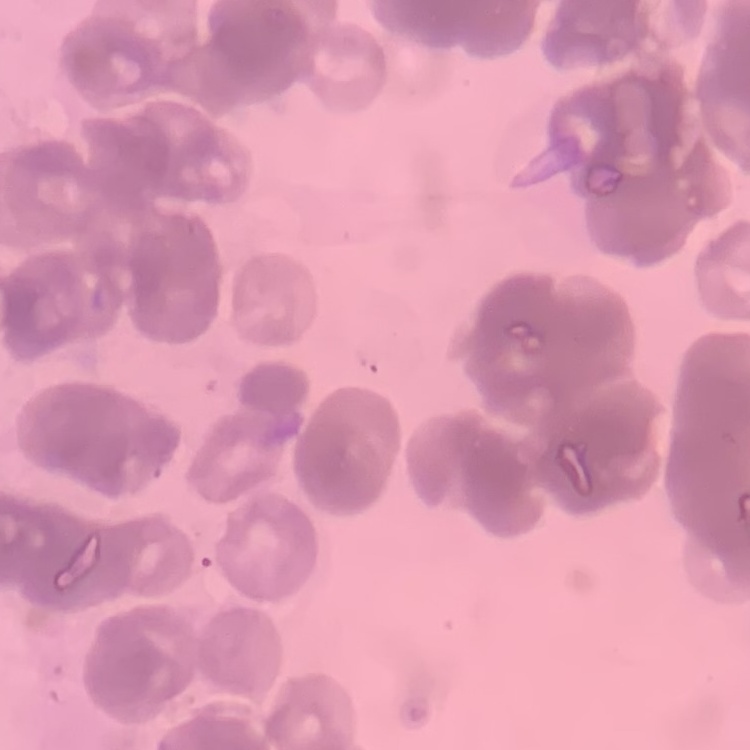

red blood cell morphology = rouleaux formation
stain = Field's or Giemsa
image type = square crop of a larger photomicrograph
preparation = thin peripheral smear